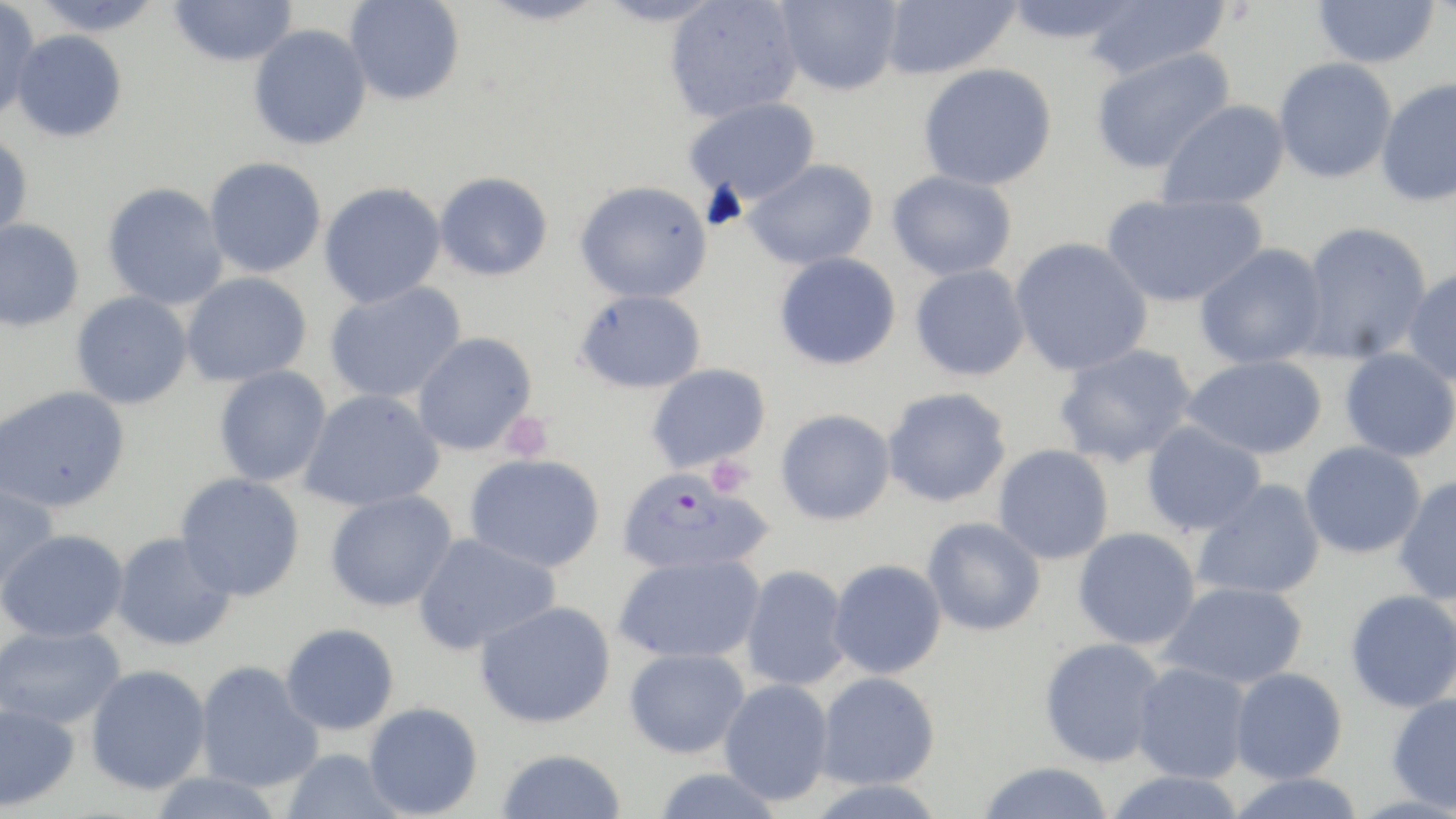
Approximate bounding boxes as [x1, y1, x2, y2] in pixels. Plasmodium falciparum-infected red blood cell locations: [617, 467, 773, 576]. Uninfected red blood cell locations: [0, 0, 41, 120], [32, 0, 164, 36], [168, 0, 297, 67], [344, 0, 465, 105], [477, 0, 607, 26], [594, 0, 725, 27], [664, 0, 803, 123], [775, 0, 903, 96], [879, 0, 1020, 79], [1003, 0, 1146, 45], [1081, 0, 1230, 80], [1312, 0, 1441, 69], [248, 23, 372, 150], [11, 29, 127, 142], [1089, 46, 1235, 174], [1273, 57, 1398, 184], [918, 63, 1058, 190], [1375, 76, 1456, 207], [684, 97, 820, 205], [1157, 99, 1290, 211], [0, 131, 33, 243], [204, 157, 327, 278], [743, 159, 880, 271], [887, 169, 1017, 280], [433, 171, 554, 281], [575, 180, 713, 303], [102, 182, 229, 310], [318, 182, 447, 308], [1101, 191, 1268, 308], [0, 218, 85, 332], [1297, 220, 1433, 364], [1008, 237, 1153, 376], [1194, 243, 1328, 369], [774, 252, 901, 370], [910, 264, 1030, 381], [1402, 266, 1456, 386], [181, 272, 312, 387], [324, 281, 466, 404], [575, 289, 707, 393], [71, 291, 193, 409], [412, 332, 538, 456], [1053, 342, 1198, 469], [1340, 347, 1456, 462], [1182, 354, 1329, 460], [646, 363, 771, 473], [213, 365, 332, 487], [1, 385, 131, 513], [883, 387, 1012, 507], [298, 388, 445, 512], [775, 408, 896, 525], [1141, 420, 1266, 536], [1299, 440, 1426, 559], [993, 444, 1114, 564], [465, 453, 606, 573], [175, 472, 305, 601], [1393, 475, 1456, 605], [1192, 478, 1326, 600], [0, 479, 60, 596], [325, 489, 458, 612], [922, 517, 1046, 636], [1073, 527, 1201, 650], [1, 528, 129, 642], [110, 531, 237, 651], [412, 532, 561, 655], [614, 552, 765, 664], [828, 559, 947, 679], [740, 564, 852, 691], [1160, 581, 1308, 689], [1345, 589, 1456, 713], [475, 600, 617, 729], [280, 622, 400, 735], [0, 624, 126, 729], [1039, 637, 1166, 767], [623, 647, 750, 758], [195, 659, 324, 792], [1131, 661, 1252, 783], [85, 664, 211, 794], [1229, 667, 1348, 783], [815, 671, 940, 790], [718, 678, 833, 806], [1387, 693, 1456, 813], [363, 701, 483, 818], [0, 702, 80, 812], [281, 748, 406, 819], [496, 748, 626, 819], [977, 761, 1115, 819], [653, 766, 784, 819], [1103, 769, 1246, 819], [146, 771, 287, 819], [1225, 772, 1366, 819], [805, 778, 948, 818]. Platelet locations: [500, 411, 553, 462], [706, 455, 754, 497]. Slide-level diagnosis: Plasmodium falciparum. Image is 1456×819 pixels. 1000x magnification. Light microscopy. Thin blood smear. May-Grünwald-Giemsa stain. Single field of view.